Classify this cell by malaria status.
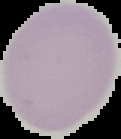
It is uninfected.

Summary:
  - Preparation: thin blood film
  - Image size: 121×139 pixels
  - Image type: segmented cell region with the area outside set to black